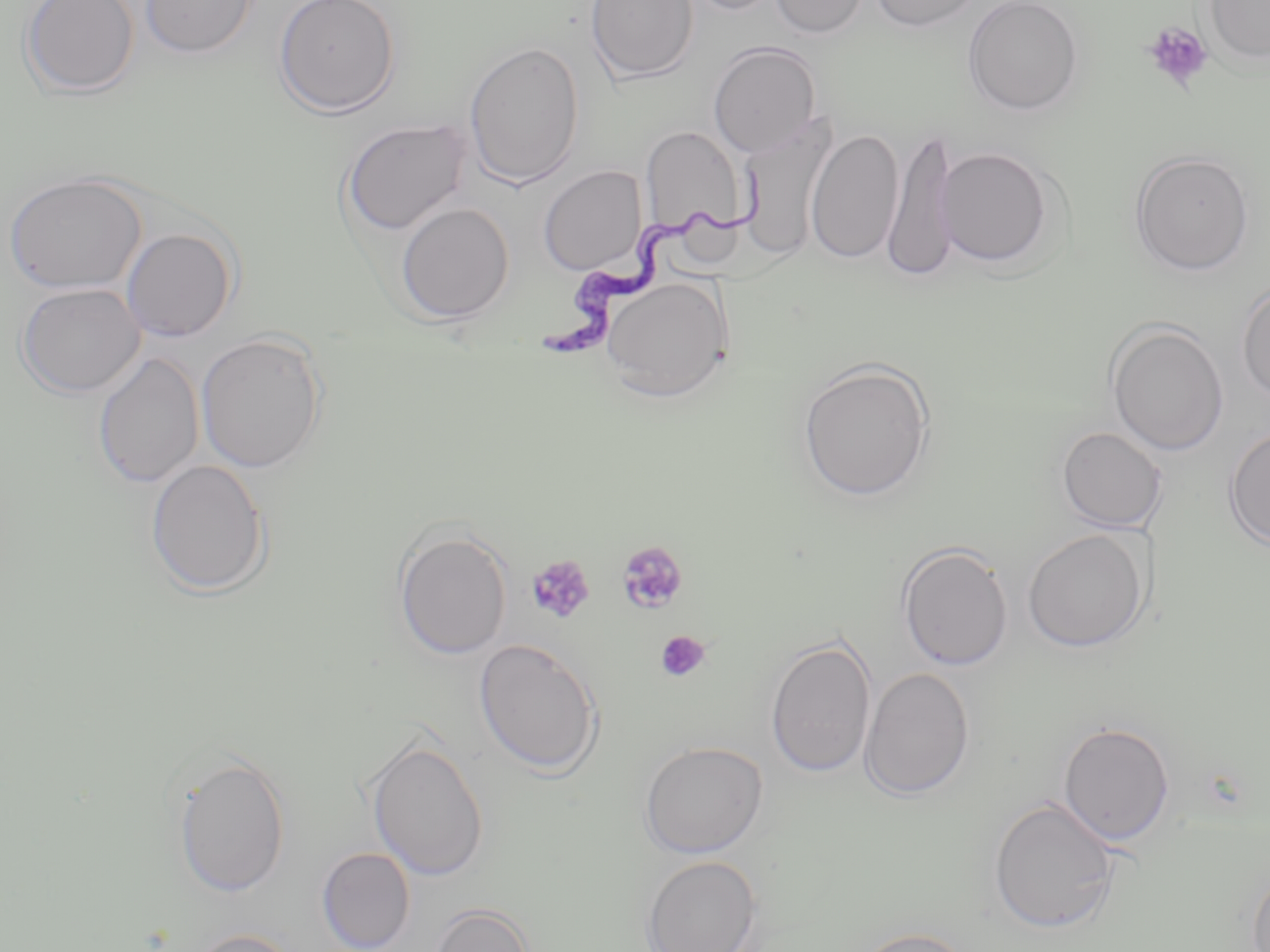 Approximate bounding boxes as [x1, y1, x2, y2] in pixels. Trypanosoma brucei locations: [537, 173, 770, 364]. Uninfected red blood cell locations: [20, 0, 140, 98], [139, 0, 259, 59], [274, 0, 401, 117], [585, 0, 699, 83], [677, 0, 787, 16], [769, 0, 870, 38], [870, 0, 984, 32], [962, 0, 1084, 116], [1203, 0, 1270, 66], [464, 39, 584, 190], [708, 42, 822, 157], [340, 118, 471, 236], [737, 118, 837, 263], [640, 125, 747, 238], [883, 126, 958, 286], [806, 128, 903, 265], [936, 145, 1056, 269], [1129, 150, 1254, 276], [538, 165, 647, 275], [5, 172, 147, 294], [395, 201, 515, 324], [120, 226, 238, 342], [600, 277, 733, 403], [1236, 281, 1270, 405], [16, 282, 145, 398], [1106, 320, 1229, 457], [196, 333, 328, 473], [93, 352, 205, 489], [797, 359, 936, 503], [1056, 426, 1168, 532], [1223, 426, 1270, 551], [145, 459, 271, 597], [392, 526, 512, 660], [1022, 528, 1150, 652], [897, 541, 1014, 671], [765, 635, 877, 779], [473, 637, 603, 777], [859, 667, 975, 800], [1058, 720, 1175, 845], [365, 735, 490, 881], [638, 740, 768, 858], [171, 752, 291, 898], [987, 796, 1121, 934], [316, 847, 415, 952], [640, 855, 763, 952], [1246, 862, 1270, 951], [429, 903, 534, 952], [850, 926, 977, 952], [187, 928, 300, 952]. Platelet locations: [1142, 21, 1213, 92], [616, 540, 690, 615], [526, 554, 595, 623], [655, 630, 712, 683]. Slide-level diagnosis: Trypanosoma brucei. Optical microscopy. May-Grünwald-Giemsa-stained preparation. Single field of view. Captured at 1000x magnification. Image is 1270×952 pixels. Thin blood smear.